Classify this cell by malaria status.
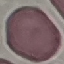
It is uninfected.

image type = cell patch, automatically extracted from a larger field of view and resized to 64 × 64 pixels
stain = Giemsa
preparation = thin blood film
capture = smartphone camera at the microscope eyepiece